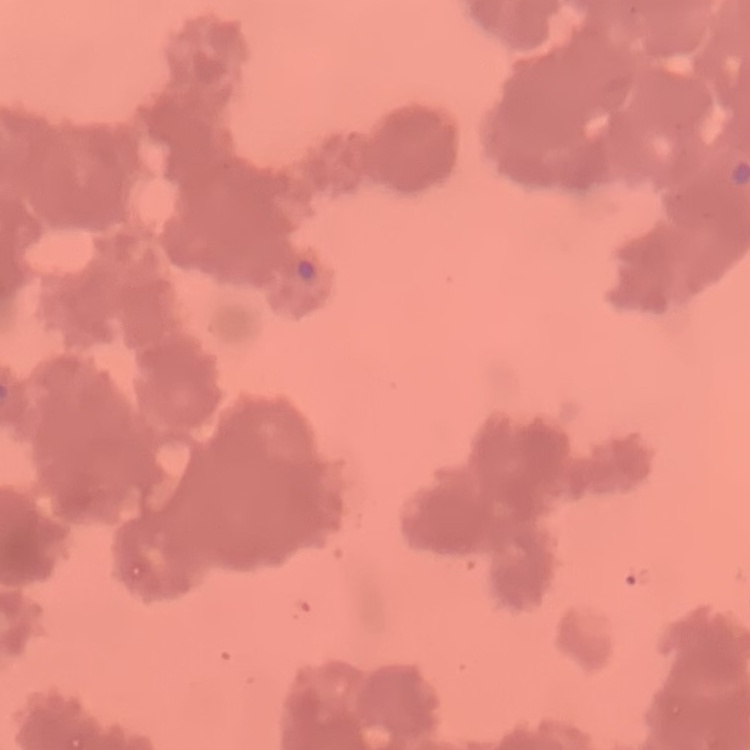
Summary:
  - Erythrocyte morphology: rouleaux formation
  - Stain: Field's or Giemsa
  - Image type: one tile cut from a larger photomicrograph
  - Preparation: thin peripheral smear